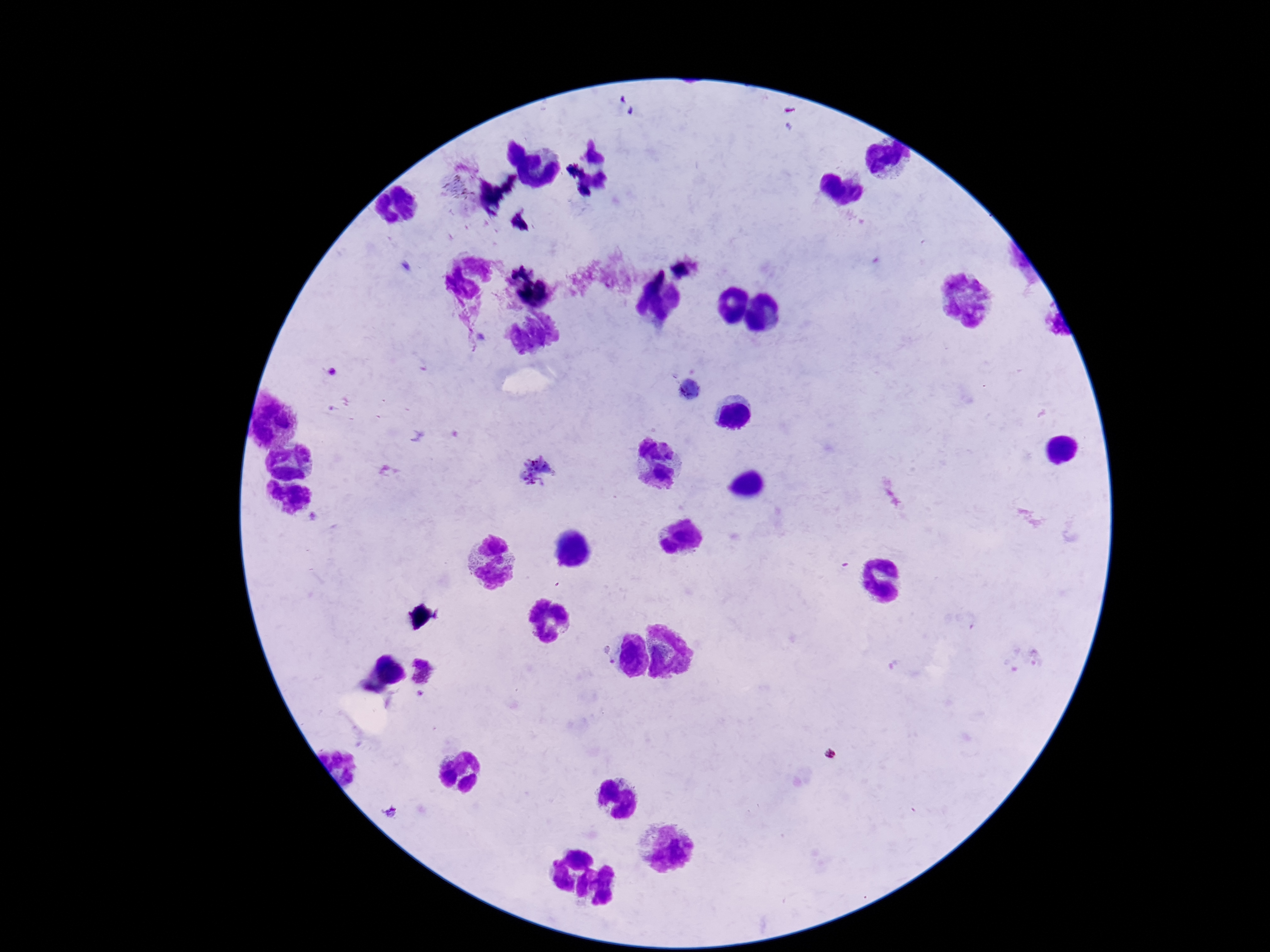
image size = 1270×952 pixels
patient malaria status = infected
capture = smartphone camera through the microscope eyepiece
field of view = single
Plasmodium parasite locations = approximate centers as [x, y] in pixels: [691, 390], [536, 472], [606, 657]
stain = Giemsa
preparation = thick blood film
magnification = 100x